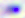

modality = photomicrograph
magnification = 400x
identification = Toxoplasma gondii